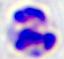

Summary:
  - Identification: leukocyte
  - Modality: micrograph
  - Magnification: 400x